Outline each Plasmodium falciparum-infected red blood cell.
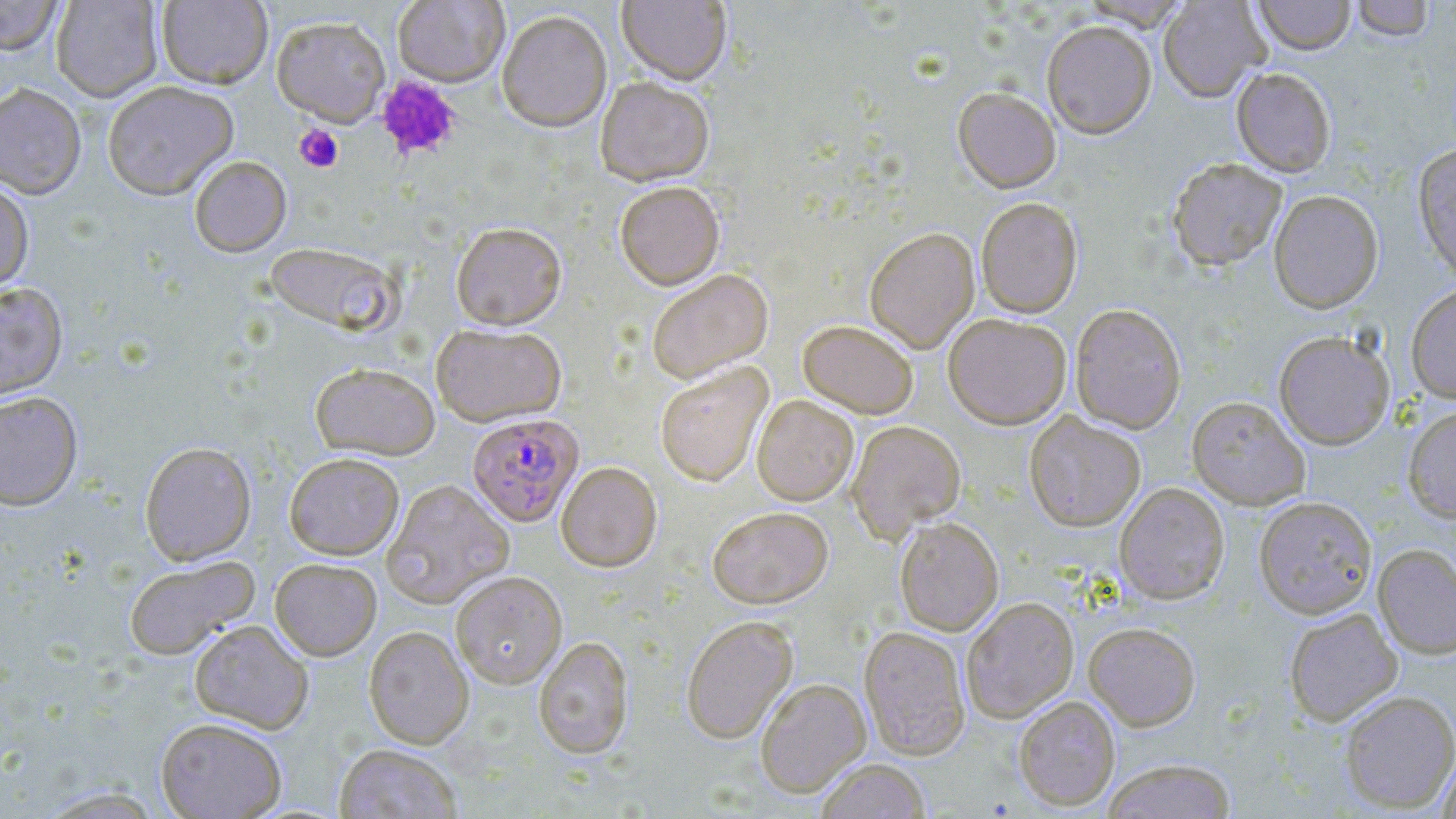

Approximate bounding boxes as (x1,y1)-(x2,y2) corner pairs in pixels.
Plasmodium falciparum-infected red blood cells: (467,413)-(582,526).

Uninfected red blood cell locations (subset): (0,0)-(65,56), (51,0)-(163,102), (156,0)-(273,88), (617,0)-(732,87), (1080,0)-(1189,33), (1158,0)-(1270,104), (1254,0)-(1355,57), (1352,1)-(1433,43), (497,10)-(612,132), (272,16)-(391,127), (1042,24)-(1156,142), (1231,69)-(1336,178), (595,77)-(714,187), (102,80)-(239,199), (0,82)-(86,199), (953,89)-(1061,196), (1412,145)-(1456,285), (189,155)-(291,256), (1168,161)-(1287,273), (0,177)-(34,296), (614,183)-(724,291), (1269,192)-(1383,315), (976,200)-(1083,319), (451,221)-(566,330), (864,229)-(980,355), (264,242)-(402,336), (647,270)-(773,384), (0,280)-(68,401), (1406,284)-(1456,405), (1070,305)-(1186,434), (943,316)-(1071,432), (798,322)-(918,420), (431,323)-(567,427), (1274,333)-(1395,450), (310,362)-(440,460), (655,362)-(773,488), (0,391)-(83,510), (752,396)-(859,507), (1186,398)-(1310,511), (1402,405)-(1456,524), (1024,412)-(1145,533), (847,422)-(966,542), (140,441)-(256,564), (284,452)-(404,559), (556,462)-(662,573), (381,480)-(514,609), (1114,484)-(1229,605), (1254,498)-(1377,620), (708,508)-(833,609), (895,519)-(1004,636), (1373,545)-(1456,659), (123,555)-(259,660), (270,558)-(382,660), (451,572)-(567,689), (962,599)-(1078,723), (1284,610)-(1402,726), (681,617)-(798,744), (189,620)-(313,734), (1084,624)-(1200,731), (363,626)-(474,748), (859,627)-(970,760), (533,636)-(634,760), (755,679)-(871,798), (1340,691)-(1456,813), (1014,697)-(1120,811), (156,717)-(286,819), (335,744)-(462,818), (1436,752)-(1456,818), (815,760)-(930,819), (1103,760)-(1236,819). Platelet locations (subset): (376,76)-(461,160), (294,124)-(344,173). Slide-level diagnosis: Plasmodium falciparum. May-Grünwald-Giemsa-stained preparation. Image is 1456×819 pixels. Optical microscopy. 1000x magnification. Single field of view. Thin blood smear.